Assess this cell for malaria.
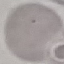
It is uninfected.

{
  "capture": "smartphone through the microscope eyepiece",
  "preparation": "thin blood smear",
  "stain": "Giemsa",
  "image_type": "automatically extracted cell patch, resized to 64 × 64 pixels"
}